Assess this cell for malaria.
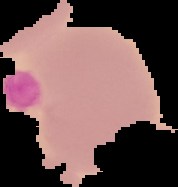
It is uninfected.

image_type: segmented cell region on a black background
preparation: thin blood film
image_size: 178×187 pixels